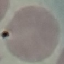 Malaria status: uninfected. Giemsa-stained preparation. Thin blood smear. Acquired by smartphone through the microscope eyepiece. Cell patch, automatically extracted from a larger field of view and resized to 64 × 64 pixels.